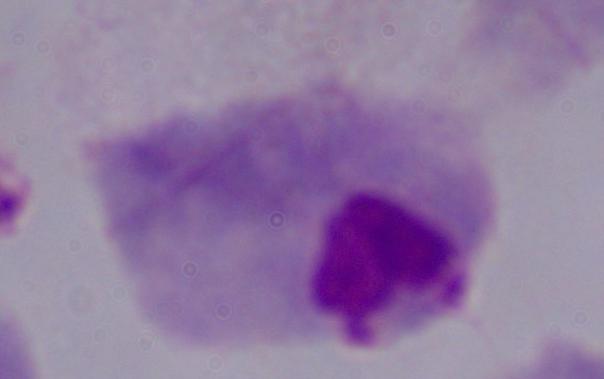

Summary:
  - Modality: photomicrograph
  - Magnification: 1000x
  - Identification: trichomonad